Assess for malaria.
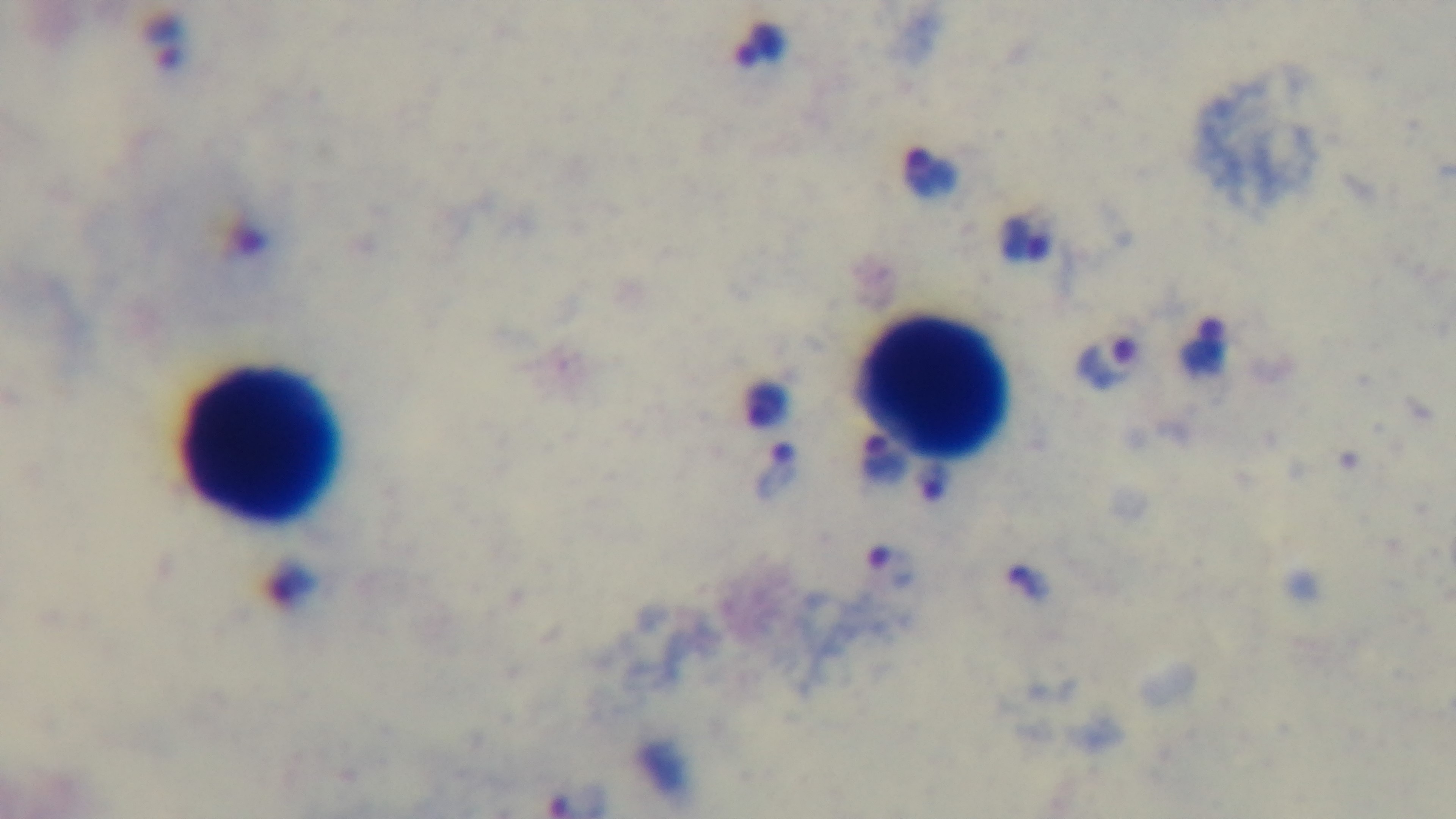
Positive.

Giemsa stain. Light microscopy. Oil-immersion objective, 100x. One field from the slide. Captured with a mounted 4K digital camera. Preparation: thick.